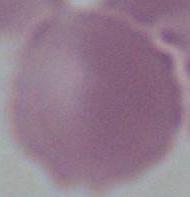

Photomicrograph. Captured at 1000x magnification. An erythrocyte is shown.